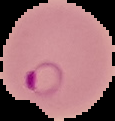

Malaria status: parasitized. From a thin blood smear. Image is 115×121 pixels. Cell region segmented out of the field of view; the surrounding area is masked to black.